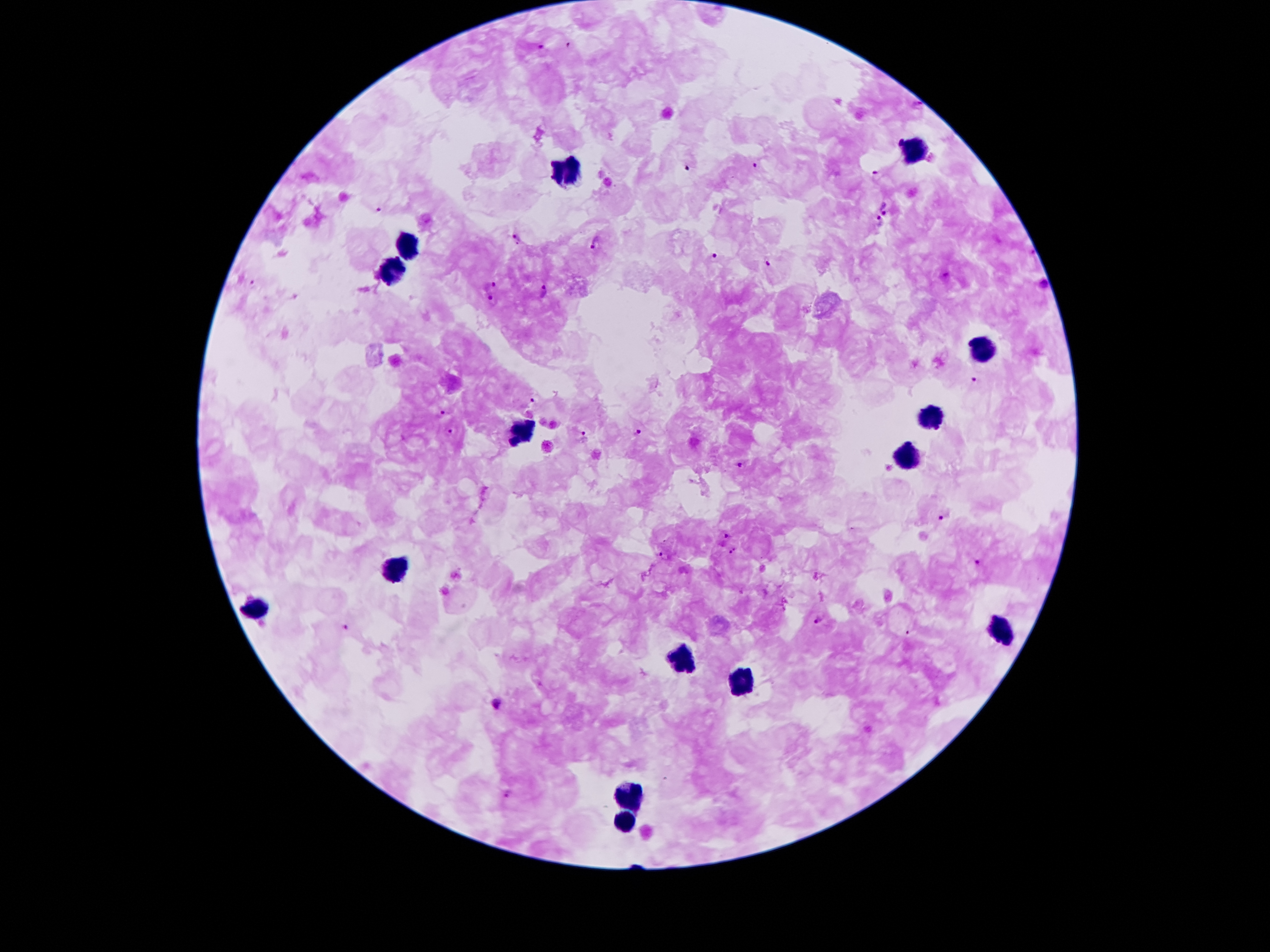
Approximate centers as (x, y) in pixels.
Summary:
  - Leukocyte locations: (914, 147), (566, 171), (409, 247), (392, 273), (978, 349), (930, 418), (524, 431), (904, 455), (395, 567), (256, 609), (1001, 630), (686, 661), (744, 682), (631, 791), (623, 821)
  - Plasmodium parasite locations: (571, 44), (540, 48), (897, 140), (686, 166), (757, 166), (876, 175), (378, 208), (886, 209), (878, 223), (517, 237), (596, 242), (714, 255), (766, 262), (253, 283), (491, 283), (1043, 286), (546, 292), (493, 301), (978, 381), (533, 402), (439, 414), (451, 430), (639, 433), (582, 436), (739, 465), (946, 517), (726, 535), (732, 548), (665, 553), (978, 564), (817, 620), (345, 625), (908, 629), (497, 704), (508, 790)
  - Magnification: 100x
  - Stain: Giemsa
  - Capture: smartphone camera through the microscope eyepiece
  - Patient malaria status: infected with Plasmodium falciparum
  - Image size: 1270×952 pixels
  - Field of view: one from this slide
  - Preparation: thick blood film